Give the position of every Plasmodium parasite.
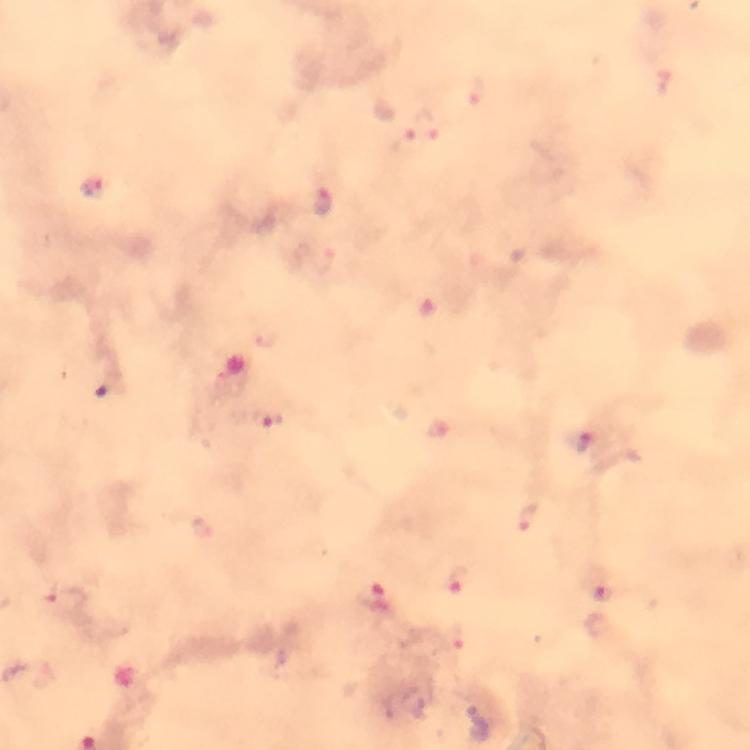
Approximate centers as {x, y} in pixels.
Plasmodium parasites: {423, 127}, {96, 187}, {323, 202}, {269, 420}, {583, 444}, {460, 585}, {601, 592}, {66, 597}, {373, 598}.

Giemsa stain. Immersion oil was used. Image is 750×750 pixels. Smartphone photograph taken through a microscope. At 100x magnification. From a malaria diagnostic workup. Thick blood smear. Cropped region of a single field of view.